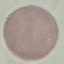

Result: no malaria parasites detected. Giemsa stain. Automatically extracted cell patch, resized to 64 × 64 pixels. Photographed with a smartphone camera at the microscope eyepiece. Thin blood smear.